Report the malaria status of this cell.
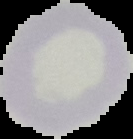

Uninfected.

Summary:
  - Preparation: thin blood film
  - Image size: 133×139 pixels
  - Image type: cell region segmented out of the field of view; surrounding area masked to black